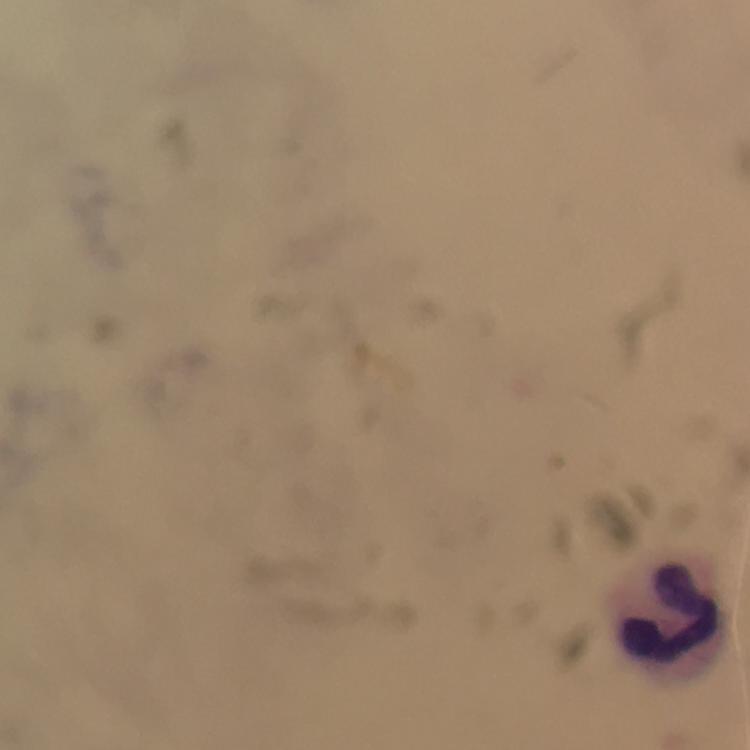

Approximate centers as (x, y) in pixels. Leukocyte locations: (670, 614). Plasmodium parasites: none detected. Giemsa-stained preparation. From a malaria diagnostic workup. Thick blood smear. A crop from one field of view. At 100x magnification. Photographed with a smartphone mounted on the microscope. Immersion oil was used. Image is 750×750 pixels.